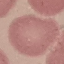 Result: negative for malaria parasites. Photographed with a smartphone camera at the microscope eyepiece. Thin blood film. Giemsa-stained preparation. Automatically extracted cell patch, resized to 64 × 64 pixels.